Identify the parasite.
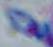

This is Toxoplasma gondii.

magnification = 1000x
modality = micrograph